Give the position of every malaria parasite.
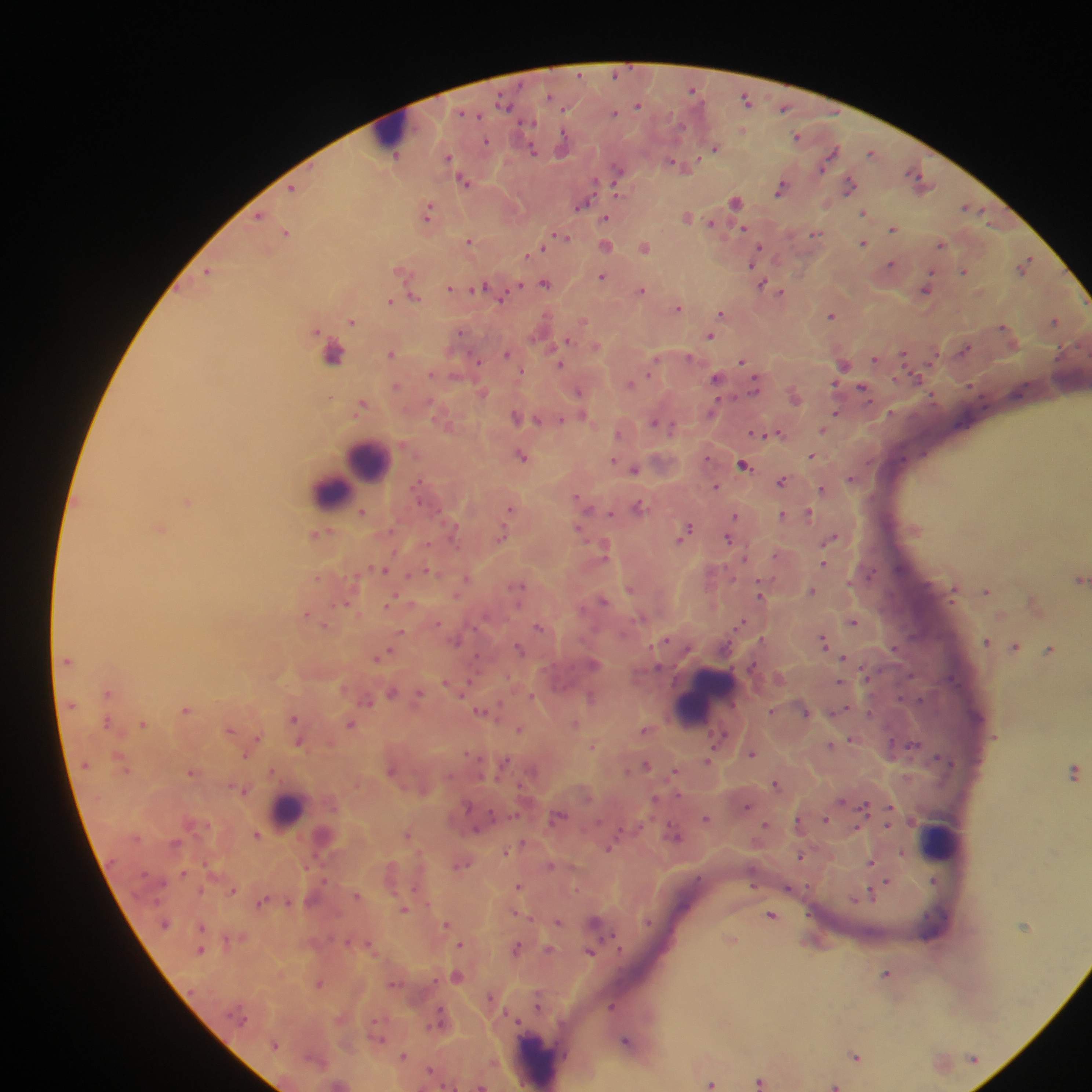
Approximate centers as {x, y} in pixels.
Malaria parasites: {616, 74}, {693, 90}, {746, 100}, {505, 103}, {638, 105}, {784, 108}, {565, 110}, {464, 113}, {614, 113}, {528, 122}, {681, 126}, {743, 130}, {797, 136}, {485, 141}, {564, 144}, {716, 148}, {533, 150}, {872, 152}, {831, 154}, {449, 157}, {395, 159}, {674, 163}, {681, 165}, {618, 169}, {915, 173}, {919, 179}, {464, 181}, {594, 183}, {849, 185}, {293, 188}, {780, 189}, {735, 200}, {583, 204}, {965, 207}, {428, 212}, {864, 212}, {259, 216}, {687, 217}, {606, 218}, {711, 223}, {743, 228}, {894, 229}, {286, 233}, {815, 233}, {563, 237}, {470, 240}, {863, 243}, {606, 245}, {940, 245}, {645, 247}, {758, 247}, {543, 248}, {530, 253}, {755, 256}, {1027, 260}, {752, 263}, {891, 264}, {963, 271}, {209, 272}, {602, 276}, {545, 284}, {763, 284}, {519, 286}, {480, 287}, {450, 288}, {927, 289}, {642, 290}, {781, 292}, {414, 296}, {500, 299}, {390, 301}, {678, 307}, {722, 313}, {831, 315}, {352, 321}, {583, 321}, {1054, 321}, {1002, 327}, {460, 333}, {710, 336}, {566, 340}, {596, 346}, {965, 349}, {334, 354}, {391, 354}, {507, 354}, {904, 354}, {688, 356}, {875, 359}, {477, 361}, {743, 361}, {561, 365}, {844, 365}, {649, 371}, {431, 373}, {717, 378}, {917, 378}, {629, 384}, {396, 386}, {755, 386}, {863, 387}, {579, 391}, {482, 392}, {429, 403}, {361, 405}, {714, 408}, {835, 414}, {516, 416}, {583, 417}, {538, 420}, {562, 420}, {654, 422}, {672, 427}, {824, 430}, {756, 432}, {779, 433}, {618, 434}, {522, 455}, {811, 455}, {613, 460}, {743, 464}, {634, 469}, {851, 478}, {782, 482}, {716, 486}, {822, 489}, {577, 497}, {187, 501}, {584, 506}, {640, 506}, {511, 508}, {362, 512}, {611, 513}, {783, 514}, {808, 514}, {736, 515}, {160, 529}, {579, 530}, {686, 530}, {453, 531}, {502, 536}, {682, 538}, {729, 538}, {832, 539}, {604, 549}, {776, 554}, {744, 558}, {826, 559}, {824, 564}, {384, 569}, {427, 571}, {871, 575}, {318, 578}, {1080, 578}, {466, 579}, {520, 585}, {629, 589}, {812, 590}, {987, 591}, {954, 593}, {457, 594}, {760, 594}, {603, 600}, {391, 602}, {346, 603}, {306, 614}, {742, 621}, {437, 622}, {854, 622}, {538, 627}, {402, 631}, {663, 640}, {457, 641}, {986, 641}, {823, 642}, {1016, 646}, {519, 648}, {894, 648}, {1050, 650}, {385, 653}, {379, 657}, {843, 658}, {67, 661}, {594, 664}, {658, 667}, {446, 681}, {471, 682}, {839, 682}, {108, 692}, {392, 692}, {419, 694}, {531, 697}, {591, 697}, {921, 700}, {367, 701}, {185, 710}, {772, 710}, {481, 711}, {840, 711}, {869, 712}, {806, 713}, {293, 718}, {107, 722}, {143, 724}, {350, 724}, {575, 724}, {230, 730}, {519, 730}, {645, 730}, {720, 736}, {851, 740}, {299, 743}, {593, 745}, {831, 745}, {912, 746}, {752, 754}, {244, 755}, {708, 760}, {505, 761}, {646, 766}, {272, 770}, {391, 770}, {191, 771}, {1074, 772}, {675, 773}, {776, 784}, {241, 790}, {654, 799}, {468, 806}, {864, 806}, {746, 807}, {558, 815}, {706, 818}, {826, 819}, {798, 822}, {765, 825}, {476, 831}, {257, 835}, {408, 835}, {675, 835}, {609, 848}, {505, 850}, {800, 857}, {871, 862}, {461, 865}, {551, 865}, {183, 873}, {934, 880}, {888, 882}, {518, 886}, {788, 889}, {233, 891}, {356, 895}, {870, 896}, {262, 902}, {403, 909}, {771, 915}, {558, 922}, {595, 922}, {165, 923}, {446, 924}, {201, 927}, {731, 939}, {460, 945}, {517, 948}, {548, 949}, {200, 950}, {590, 953}, {886, 973}, {457, 976}, {320, 984}, {538, 1002}, {611, 1006}, {626, 1040}, {275, 1044}, {403, 1056}, {856, 1056}, {430, 1070}, {760, 1081}, {711, 1083}, {835, 1085}, {482, 1086}.

preparation = thick blood smear
capture = mobile-phone photograph through a microscope
leukocyte locations = approximate centers as {x, y} in pixels: {394, 135}, {367, 461}, {351, 477}, {331, 492}, {704, 701}, {288, 811}, {940, 839}, {539, 1062}
image size = 1092×1092 pixels
country = Ghana
field of view = single